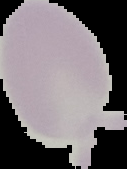 Malaria status: uninfected. The area outside the segmented cell region is set to black. From a thin blood film. Image is 127×169 pixels.